Report the malaria status of this cell.
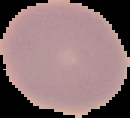
Uninfected.

Summary:
  - Preparation: thin blood smear
  - Image type: cell region segmented out of the field of view; surrounding area masked to black
  - Image size: 130×118 pixels